Outline each blood parasite and name the species.
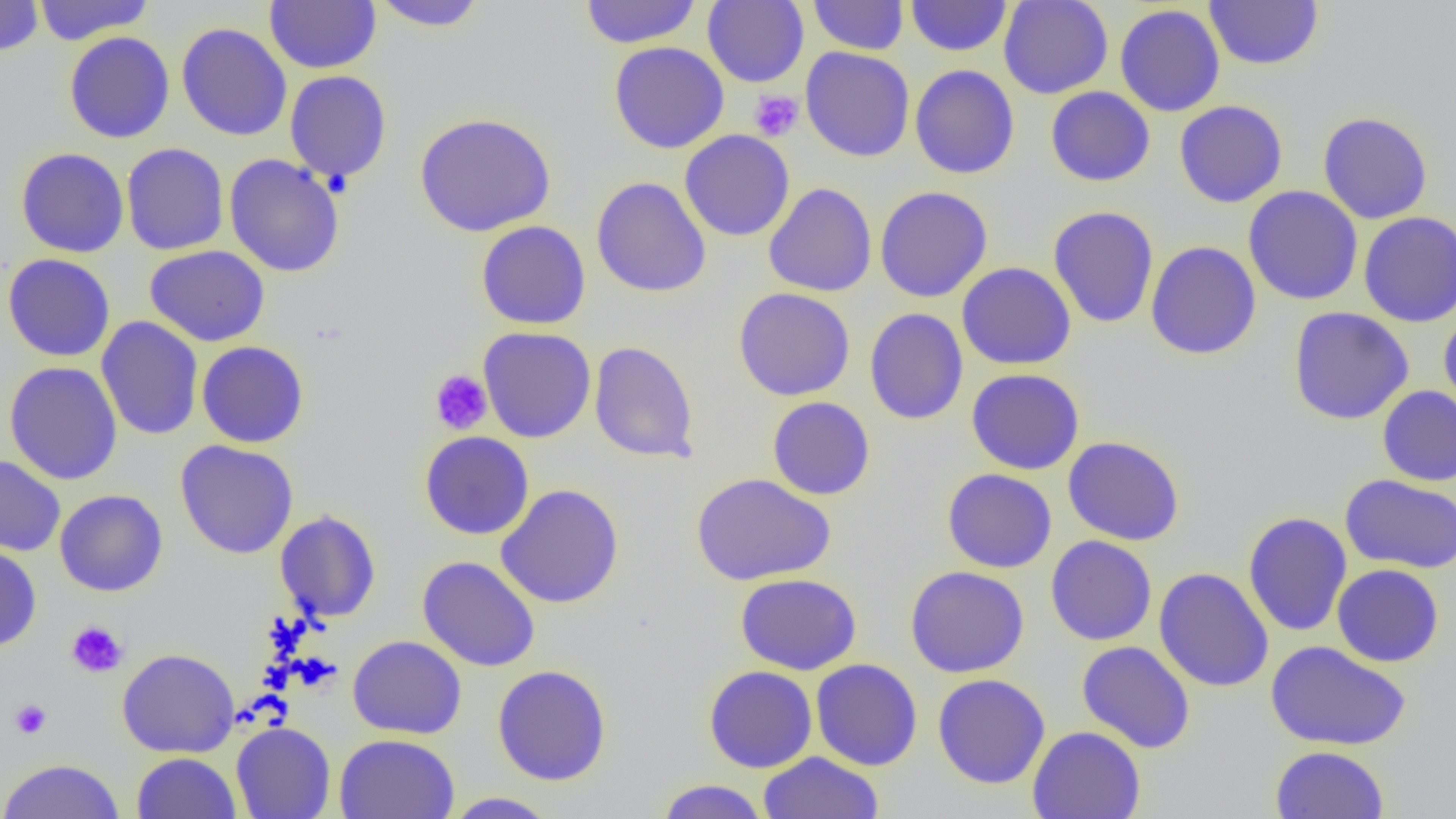

No blood parasites seen.

Approximate bounding boxes as named x1/y1/x2/y2 corners in pixels. Uninfected red blood cell locations: (x1=0, y1=0, x2=45, y2=57), (x1=580, y1=0, x2=701, y2=49), (x1=703, y1=0, x2=809, y2=87), (x1=808, y1=0, x2=908, y2=55), (x1=905, y1=0, x2=1012, y2=56), (x1=998, y1=0, x2=1113, y2=99), (x1=1204, y1=0, x2=1324, y2=71), (x1=32, y1=1, x2=153, y2=45), (x1=265, y1=1, x2=381, y2=73), (x1=369, y1=1, x2=488, y2=31), (x1=1115, y1=4, x2=1225, y2=116), (x1=176, y1=22, x2=292, y2=141), (x1=64, y1=31, x2=175, y2=143), (x1=609, y1=41, x2=729, y2=154), (x1=800, y1=46, x2=915, y2=162), (x1=909, y1=64, x2=1020, y2=179), (x1=284, y1=70, x2=392, y2=184), (x1=1045, y1=86, x2=1155, y2=186), (x1=1174, y1=100, x2=1288, y2=208), (x1=1317, y1=111, x2=1433, y2=224), (x1=414, y1=112, x2=556, y2=237), (x1=680, y1=129, x2=795, y2=242), (x1=121, y1=143, x2=229, y2=255), (x1=16, y1=147, x2=129, y2=258), (x1=224, y1=154, x2=345, y2=277), (x1=591, y1=177, x2=711, y2=298), (x1=763, y1=182, x2=877, y2=297), (x1=875, y1=186, x2=992, y2=303), (x1=1243, y1=186, x2=1363, y2=305), (x1=1047, y1=205, x2=1159, y2=329), (x1=1358, y1=211, x2=1456, y2=326), (x1=476, y1=221, x2=591, y2=329), (x1=1145, y1=241, x2=1261, y2=360), (x1=144, y1=245, x2=270, y2=346), (x1=2, y1=253, x2=116, y2=361), (x1=957, y1=262, x2=1076, y2=370), (x1=733, y1=287, x2=855, y2=401), (x1=1288, y1=307, x2=1414, y2=425), (x1=864, y1=308, x2=968, y2=425), (x1=1439, y1=310, x2=1456, y2=420), (x1=96, y1=316, x2=204, y2=441), (x1=478, y1=326, x2=596, y2=443), (x1=196, y1=341, x2=309, y2=448), (x1=589, y1=341, x2=699, y2=463), (x1=4, y1=361, x2=122, y2=485), (x1=967, y1=368, x2=1084, y2=474), (x1=1377, y1=385, x2=1456, y2=486), (x1=767, y1=396, x2=876, y2=500), (x1=419, y1=431, x2=534, y2=540), (x1=1063, y1=436, x2=1185, y2=546), (x1=175, y1=440, x2=299, y2=559), (x1=0, y1=455, x2=66, y2=556), (x1=942, y1=468, x2=1057, y2=573), (x1=690, y1=472, x2=835, y2=585), (x1=1340, y1=474, x2=1456, y2=574), (x1=496, y1=484, x2=625, y2=608), (x1=54, y1=489, x2=168, y2=596), (x1=275, y1=510, x2=381, y2=623), (x1=1243, y1=511, x2=1352, y2=636), (x1=1045, y1=535, x2=1157, y2=646), (x1=0, y1=545, x2=42, y2=653), (x1=417, y1=556, x2=540, y2=671), (x1=1332, y1=564, x2=1444, y2=667), (x1=905, y1=565, x2=1029, y2=678), (x1=1153, y1=567, x2=1274, y2=692), (x1=735, y1=573, x2=862, y2=675), (x1=348, y1=635, x2=467, y2=739), (x1=1077, y1=640, x2=1195, y2=753), (x1=1265, y1=640, x2=1412, y2=751), (x1=117, y1=648, x2=239, y2=758), (x1=811, y1=658, x2=923, y2=771), (x1=493, y1=665, x2=611, y2=786), (x1=703, y1=665, x2=818, y2=772), (x1=932, y1=673, x2=1051, y2=789), (x1=231, y1=722, x2=336, y2=819), (x1=1027, y1=726, x2=1145, y2=818), (x1=334, y1=734, x2=460, y2=819), (x1=1270, y1=745, x2=1390, y2=819), (x1=132, y1=752, x2=241, y2=818), (x1=758, y1=752, x2=884, y2=818), (x1=0, y1=758, x2=125, y2=819), (x1=654, y1=779, x2=770, y2=818), (x1=441, y1=792, x2=560, y2=818). Platelet locations: (x1=749, y1=90, x2=804, y2=142), (x1=429, y1=369, x2=493, y2=434), (x1=66, y1=620, x2=128, y2=678), (x1=10, y1=698, x2=52, y2=739). Slide-level diagnosis: no evidence of blood parasites. Thin blood film. Light microscopy. One field of a larger specimen. Captured at 1000x magnification. Image is 1456×819 pixels.